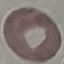

Result: negative for malaria parasites. Acquired by smartphone through the microscope eyepiece. Cell patch, automatically extracted from a larger field of view and resized to 64 × 64 pixels. Thin blood smear. Giemsa-stained preparation.